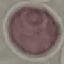

Malaria status: uninfected. Acquired by smartphone through the microscope eyepiece. Giemsa-stained preparation. Thin smear of blood. Automatically extracted cell patch, resized to 64 × 64 pixels.